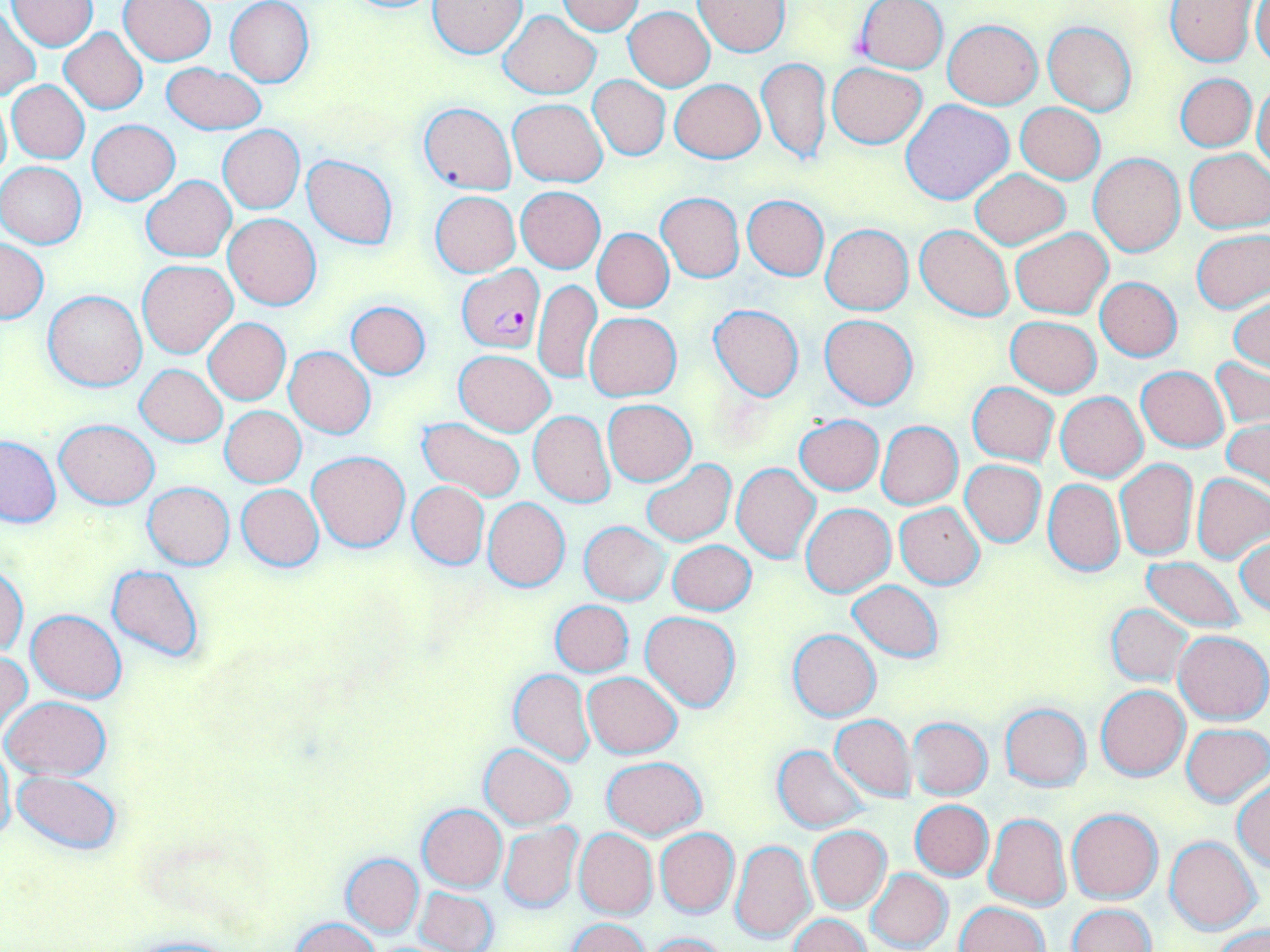

Summary:
  - Coordinate format: approximate bounding boxes as [x1, y1, x2, y2] in pixels
  - Plasmodium falciparum-infected red blood cell locations: [457, 265, 545, 353]
  - Uninfected red blood cell locations: [332, 0, 447, 15], [9, 1, 96, 50], [119, 1, 218, 65], [225, 1, 315, 86], [428, 1, 526, 57], [557, 1, 645, 35], [695, 1, 790, 55], [854, 1, 948, 74], [1165, 1, 1261, 66], [1251, 2, 1270, 69], [624, 6, 715, 90], [0, 10, 40, 101], [501, 11, 599, 98], [943, 19, 1044, 108], [1043, 20, 1137, 115], [59, 27, 148, 115], [758, 57, 830, 168], [828, 62, 926, 149], [161, 63, 266, 134], [1176, 73, 1256, 152], [588, 75, 670, 159], [670, 79, 765, 163], [8, 81, 90, 163], [1253, 81, 1269, 176], [0, 92, 11, 188], [508, 99, 607, 186], [900, 100, 1015, 206], [419, 102, 514, 194], [1015, 103, 1105, 183], [88, 120, 179, 204], [218, 125, 304, 213], [1184, 150, 1270, 232], [1089, 152, 1186, 256], [301, 155, 398, 248], [0, 162, 87, 248], [971, 169, 1070, 249], [140, 175, 236, 262], [516, 186, 604, 272], [431, 191, 520, 276], [657, 192, 744, 282], [742, 195, 829, 281], [223, 212, 321, 309], [821, 223, 914, 315], [915, 225, 1014, 322], [1010, 228, 1112, 318], [594, 229, 673, 312], [1192, 229, 1269, 313], [0, 238, 48, 323], [136, 259, 238, 358], [534, 278, 602, 383], [1096, 278, 1182, 360], [43, 291, 147, 392], [1229, 293, 1269, 374], [344, 300, 431, 378], [708, 305, 804, 401], [584, 312, 681, 401], [819, 314, 919, 409], [1005, 316, 1101, 396], [204, 318, 289, 405], [284, 346, 376, 439], [453, 349, 556, 436], [1211, 356, 1269, 431], [136, 364, 227, 446], [1137, 367, 1228, 451], [968, 382, 1058, 465], [1056, 392, 1147, 481], [603, 400, 696, 485], [221, 406, 305, 486], [529, 411, 615, 507], [793, 415, 884, 496], [416, 418, 527, 503], [54, 419, 159, 507], [1223, 420, 1270, 497], [876, 421, 963, 509], [0, 436, 62, 528], [308, 450, 409, 551], [641, 459, 735, 546], [1115, 459, 1197, 561], [961, 460, 1046, 546], [732, 463, 821, 562], [1192, 472, 1269, 562], [1043, 479, 1124, 576], [407, 481, 489, 570], [143, 482, 235, 569], [237, 483, 323, 572], [484, 498, 570, 591], [801, 503, 894, 597], [895, 503, 984, 588], [580, 521, 669, 604], [1236, 536, 1270, 617], [668, 539, 755, 614], [1140, 556, 1248, 634], [106, 564, 206, 663], [1, 566, 28, 656], [848, 581, 943, 661], [549, 599, 634, 676], [1106, 604, 1193, 686], [27, 609, 126, 703], [642, 612, 741, 712], [788, 628, 881, 721], [1174, 630, 1269, 725], [1, 650, 32, 735], [509, 669, 594, 765], [583, 672, 682, 758], [1096, 685, 1190, 780], [3, 696, 111, 779], [1000, 703, 1090, 791], [830, 715, 915, 801], [906, 717, 992, 800], [1181, 723, 1270, 806], [0, 743, 15, 850], [480, 744, 576, 829], [772, 746, 870, 833], [602, 756, 707, 838], [11, 769, 124, 854], [1232, 778, 1270, 872], [910, 800, 993, 880], [418, 805, 507, 891], [1068, 808, 1162, 903], [984, 812, 1070, 910], [498, 823, 582, 913], [806, 825, 890, 912], [574, 828, 657, 918], [655, 828, 739, 917], [1165, 837, 1262, 934], [731, 840, 815, 944], [342, 853, 425, 937], [865, 868, 953, 951], [414, 886, 499, 952], [954, 902, 1049, 952], [1067, 903, 1156, 952], [789, 914, 870, 952], [290, 917, 381, 952], [565, 919, 651, 952], [1213, 926, 1270, 952], [643, 932, 734, 952], [118, 933, 249, 952]
  - Slide-level diagnosis: Plasmodium falciparum
  - Modality: light microscopy
  - Preparation: thin blood film
  - Stain: May-Grünwald-Giemsa
  - Field of view: one of a larger specimen
  - Image size: 1270×952 pixels
  - Magnification: 1000x